Outline each blood parasite and name the species.
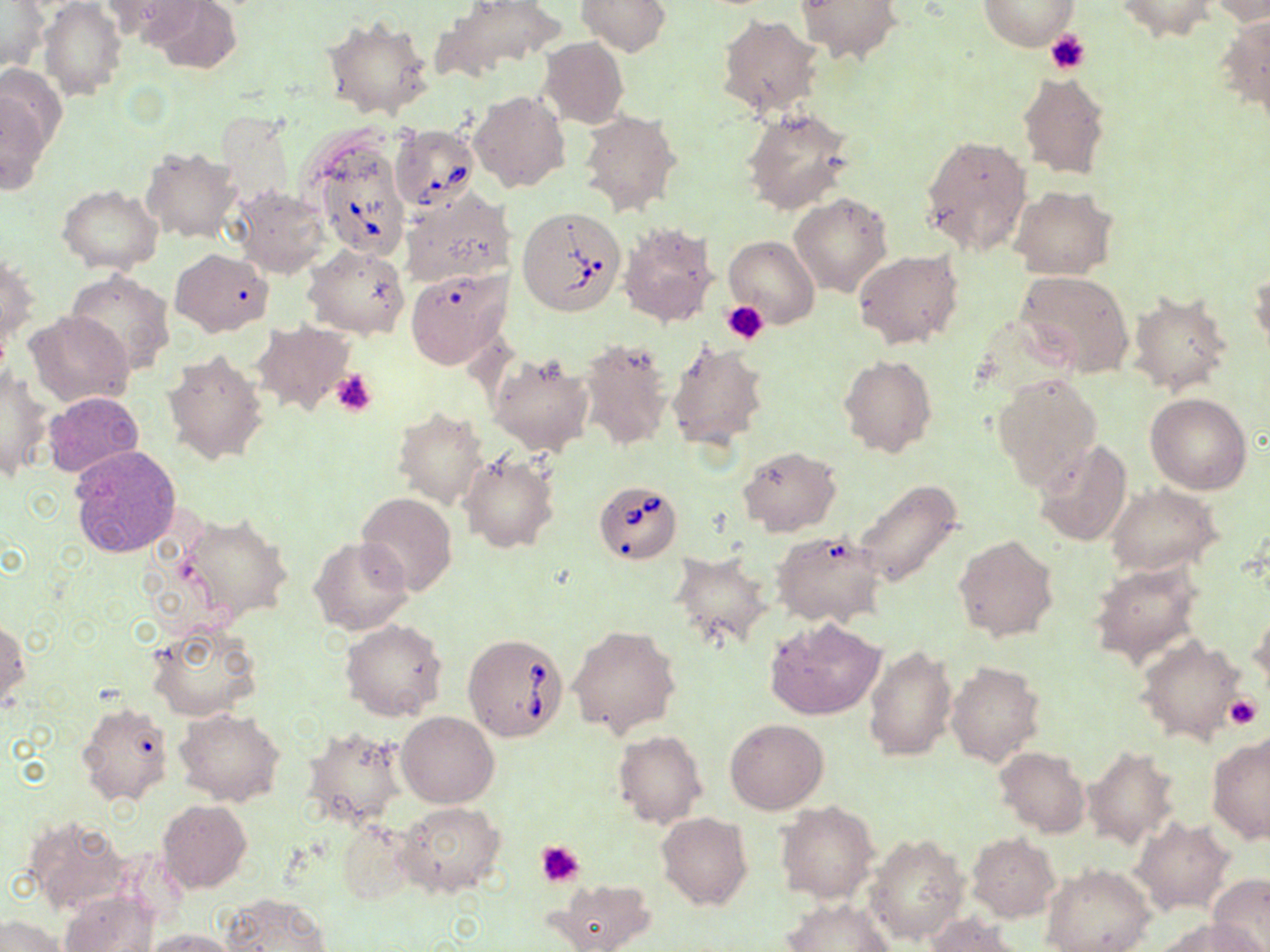
Approximate bounding boxes as [x1, y1, x2, y2] in pixels.
Babesia divergens-infected red blood cells: [390, 123, 479, 214], [310, 136, 410, 260], [518, 205, 628, 316], [593, 479, 682, 564], [462, 633, 569, 742].
No Plasmodium falciparum, Plasmodium ovale, Plasmodium malariae, Plasmodium vivax, or Trypanosoma brucei observed.

Summary:
  - Uninfected red blood cell locations: [98, 0, 201, 44], [148, 0, 244, 75], [576, 0, 671, 56], [980, 0, 1077, 51], [1114, 0, 1216, 41], [437, 1, 565, 75], [796, 1, 900, 62], [1208, 1, 1270, 25], [40, 2, 128, 101], [1, 3, 48, 75], [1218, 14, 1270, 117], [322, 16, 432, 123], [718, 16, 824, 117], [539, 37, 628, 129], [1016, 71, 1111, 179], [2, 84, 54, 195], [468, 90, 568, 192], [739, 106, 854, 215], [578, 109, 681, 215], [217, 113, 296, 203], [920, 134, 1034, 255], [142, 147, 241, 242], [59, 185, 163, 273], [233, 186, 329, 277], [1011, 186, 1116, 279], [400, 188, 517, 288], [791, 194, 893, 297], [618, 222, 718, 330], [724, 236, 819, 329], [301, 243, 410, 340], [171, 248, 274, 337], [854, 249, 964, 349], [2, 250, 37, 358], [406, 268, 510, 368], [1250, 269, 1270, 358], [66, 270, 175, 374], [1014, 271, 1135, 377], [1128, 291, 1234, 395], [26, 309, 132, 407], [252, 321, 355, 415], [578, 338, 673, 449], [666, 339, 769, 449], [162, 348, 269, 467], [488, 352, 595, 456], [838, 355, 936, 459], [1, 364, 52, 482], [992, 373, 1103, 489], [43, 390, 144, 478], [1146, 392, 1252, 494], [392, 407, 487, 508], [1034, 439, 1133, 547], [68, 443, 180, 559], [737, 446, 841, 536], [461, 453, 559, 553], [853, 478, 963, 587], [1105, 483, 1223, 575], [357, 493, 457, 595], [180, 514, 292, 623], [774, 531, 888, 628], [953, 534, 1059, 643], [310, 536, 412, 634], [669, 552, 773, 650], [1089, 561, 1203, 665], [1251, 606, 1270, 694], [767, 617, 885, 720], [340, 619, 448, 721], [146, 620, 261, 722], [0, 621, 29, 714], [568, 624, 681, 739], [1135, 635, 1249, 747], [863, 645, 957, 761], [945, 660, 1045, 766], [75, 700, 174, 810], [175, 709, 284, 806], [397, 711, 499, 807], [726, 718, 827, 813], [300, 724, 408, 827], [613, 731, 707, 828], [1206, 735, 1270, 845], [1084, 747, 1178, 847], [995, 748, 1088, 836], [157, 799, 251, 893], [397, 801, 507, 896], [777, 802, 879, 903], [658, 813, 752, 911], [25, 815, 130, 914], [1131, 817, 1234, 915], [335, 819, 416, 906], [866, 831, 969, 946], [966, 833, 1059, 921], [1042, 864, 1156, 952], [1207, 874, 1270, 951], [552, 877, 658, 952], [60, 890, 158, 952], [221, 893, 332, 952], [781, 898, 894, 951], [925, 913, 1025, 952], [1, 915, 68, 952], [1161, 921, 1267, 952], [147, 928, 239, 952]
  - Platelet locations: [1045, 30, 1091, 74], [721, 301, 770, 345], [330, 369, 378, 417], [1226, 692, 1261, 728], [536, 841, 586, 888]
  - Slide-level diagnosis: Babesia divergens
  - Modality: optical microscopy
  - Magnification: 1000x
  - Field of view: one of a larger specimen
  - Preparation: thin blood smear
  - Stain: May-Grünwald-Giemsa
  - Image size: 1270×952 pixels